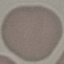

{
  "result": "negative for malaria parasites",
  "image_type": "cell patch, automatically extracted from a larger field of view and resized to 64 × 64 pixels",
  "preparation": "thin smear",
  "capture": "smartphone camera at the microscope eyepiece",
  "stain": "Giemsa"
}